Classify this cell by malaria status.
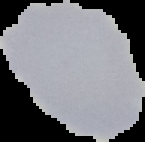
Uninfected.

Summary:
  - Image size: 145×142 pixels
  - Preparation: thin blood smear
  - Image type: cell region segmented out of the field of view; surrounding area masked to black